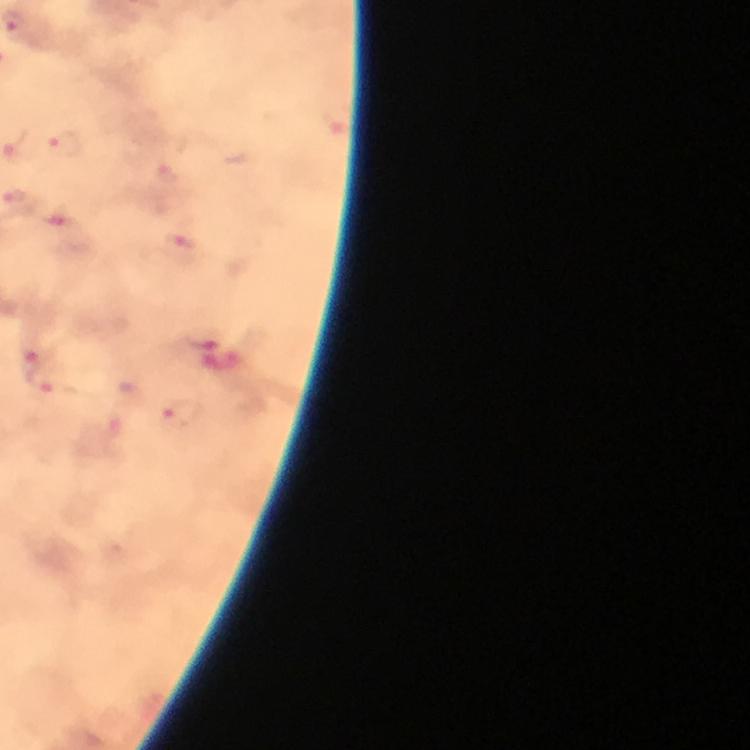
capture = smartphone mounted on the microscope
cropped from = a single field of view
preparation = thick smear
immersion oil = used
image size = 750×750 pixels
context = from a malaria diagnostic workup
stain = Giemsa
magnification = 100x
malaria parasite locations = approximate centers as {x, y} in pixels: {14, 21}, {66, 143}, {17, 148}, {180, 246}, {34, 357}, {42, 380}, {181, 413}